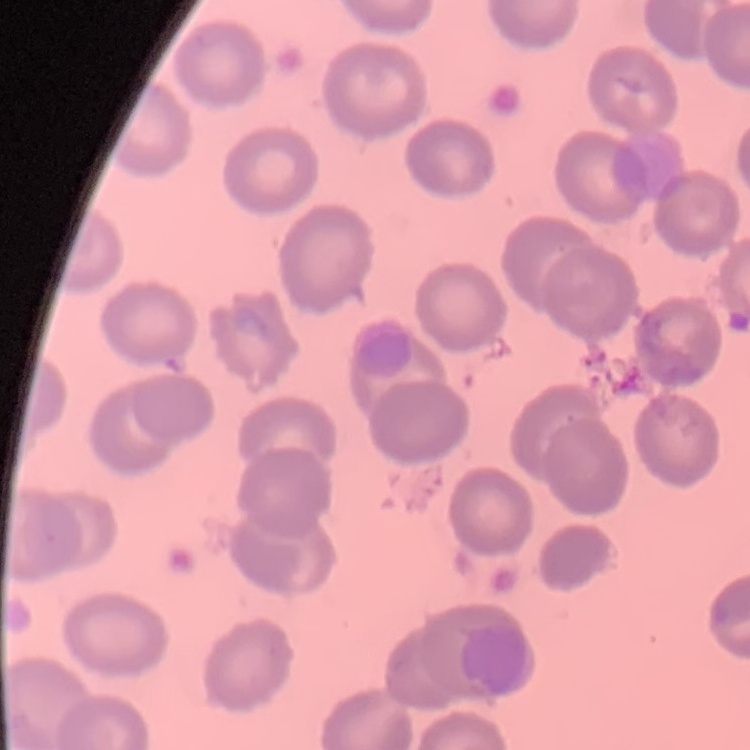

erythrocyte morphology = no rouleaux formation
preparation = thin blood smear
stain = Field's or Giemsa
image type = one tile cut from a larger photomicrograph